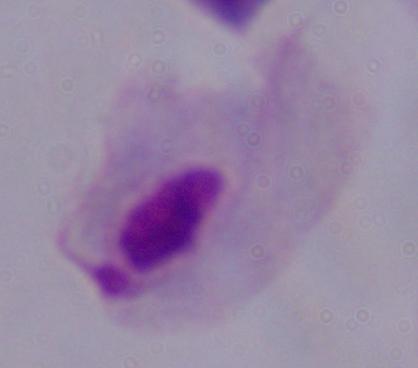
Photomicrograph. 1000x magnification. A trichomonad is shown.